Locate and identify every blood parasite.
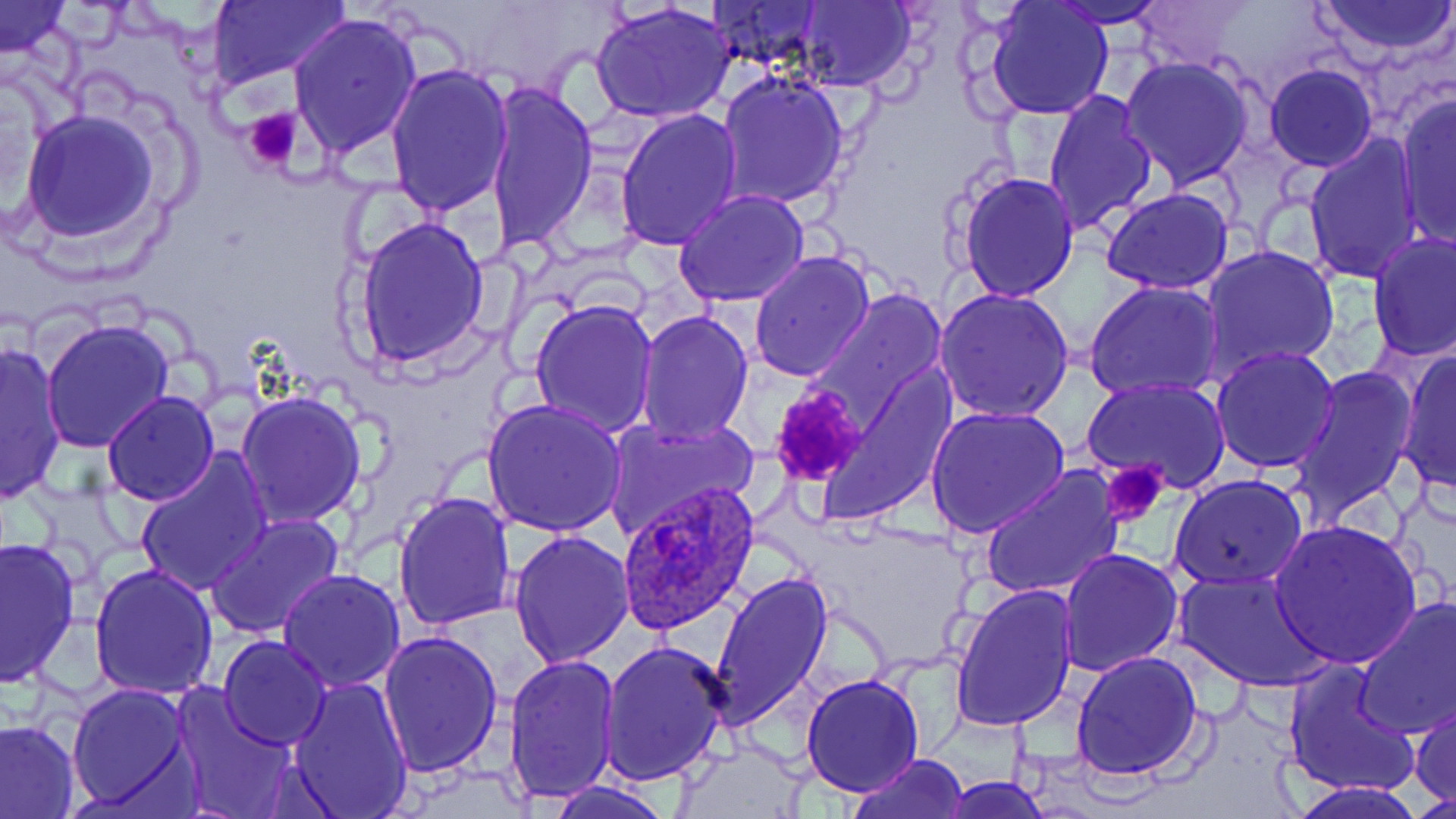
Approximate bounding boxes as (x1, y1, x2, y2) in pixels.
Plasmodium ovale-infected red blood cells: (616, 482, 762, 637).
No Plasmodium falciparum, Plasmodium malariae, Plasmodium vivax, Babesia divergens, or Trypanosoma brucei observed.

slide-level diagnosis = Plasmodium ovale
magnification = 1000x
preparation = thin blood film
uninfected red blood cell locations = approximate bounding boxes as (x1, y1, x2, y2) in pixels: (702, 0, 830, 75), (796, 0, 918, 90), (1050, 0, 1166, 28), (1134, 0, 1242, 69), (1313, 0, 1455, 58), (206, 1, 351, 89), (985, 1, 1114, 119), (0, 2, 72, 56), (593, 2, 737, 123), (287, 12, 422, 160), (1121, 55, 1255, 190), (385, 63, 515, 219), (1264, 63, 1378, 171), (716, 69, 850, 209), (482, 81, 599, 253), (1042, 90, 1157, 237), (1395, 93, 1455, 249), (18, 109, 163, 245), (615, 109, 744, 251), (1303, 132, 1426, 284), (955, 169, 1079, 303), (1100, 187, 1235, 294), (673, 190, 811, 309), (350, 214, 493, 370), (1368, 233, 1455, 362), (1201, 244, 1341, 379), (749, 250, 875, 381), (1084, 281, 1225, 403), (933, 287, 1076, 423), (802, 288, 950, 437), (529, 297, 658, 438), (635, 308, 755, 447), (39, 318, 175, 453), (0, 341, 67, 502), (1211, 346, 1339, 473), (1397, 351, 1455, 494), (813, 365, 957, 520), (1288, 366, 1419, 522), (1082, 380, 1230, 495), (235, 389, 367, 528), (100, 390, 219, 507), (481, 400, 629, 540), (926, 405, 1068, 541), (601, 413, 760, 540), (134, 447, 273, 596), (980, 464, 1123, 601), (1169, 472, 1309, 590), (392, 491, 519, 633), (205, 513, 345, 639), (1267, 520, 1424, 669), (507, 529, 635, 669), (1, 537, 79, 687), (1059, 549, 1184, 677), (89, 564, 220, 702), (1173, 567, 1332, 691), (277, 568, 406, 693), (709, 571, 834, 730), (948, 583, 1077, 731), (1353, 596, 1456, 738), (234, 598, 378, 725), (377, 631, 504, 778), (218, 636, 332, 750), (599, 638, 730, 787), (1070, 651, 1204, 781), (502, 653, 619, 806), (1284, 659, 1419, 800), (801, 672, 924, 795), (287, 676, 413, 815), (170, 683, 298, 819), (66, 684, 192, 810), (1410, 697, 1455, 807), (0, 719, 80, 818), (674, 744, 808, 817), (846, 753, 972, 818), (936, 776, 1055, 817), (543, 780, 671, 819), (1288, 781, 1427, 819)
modality = light microscopy
stain = May-Grünwald-Giemsa
field of view = single
platelet locations = approximate bounding boxes as (x1, y1, x2, y2) in pixels: (242, 107, 304, 174), (768, 388, 867, 487), (1100, 461, 1170, 527)
image size = 1456×819 pixels